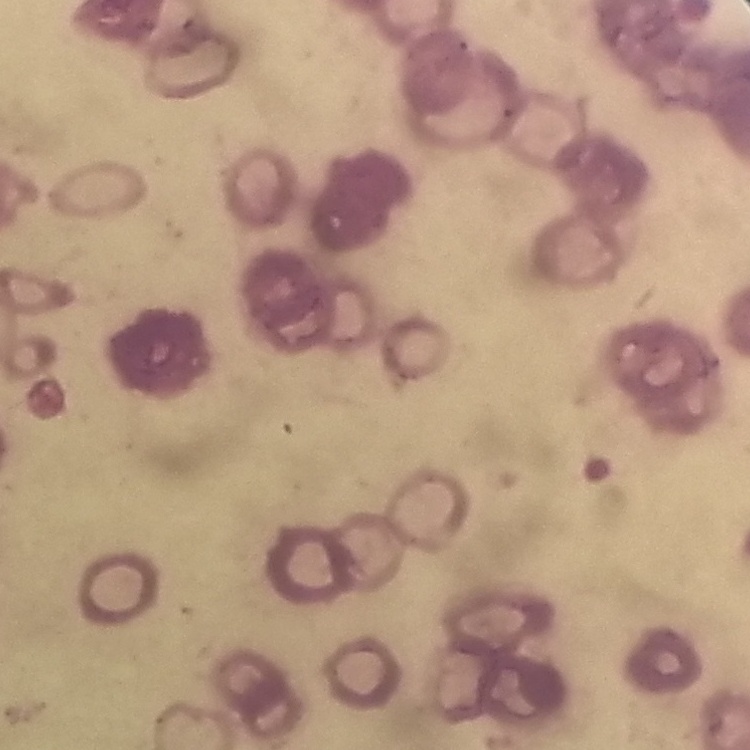 The erythrocytes exhibit rouleaux formation. Square crop of a larger photomicrograph. Thin blood film. Field's or Giemsa stain.